Identify the preparation type.
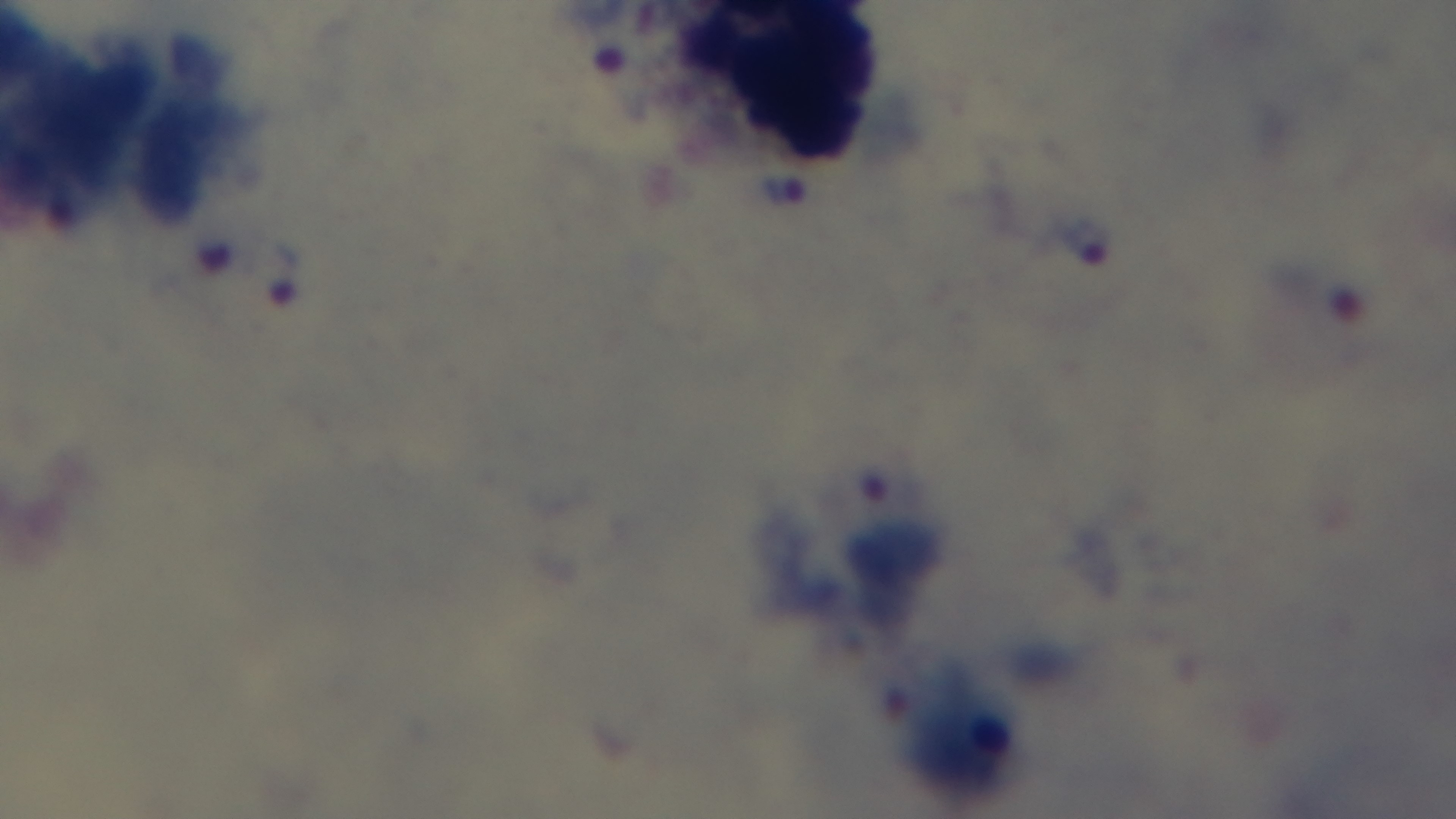

It is a thick blood film.

capture = mounted 4K digital camera
field of view = one from the slide
malaria status = infected
objective = 100x oil immersion
modality = light microscopy
stain = Giemsa